Assess the morphology of the red blood cells.
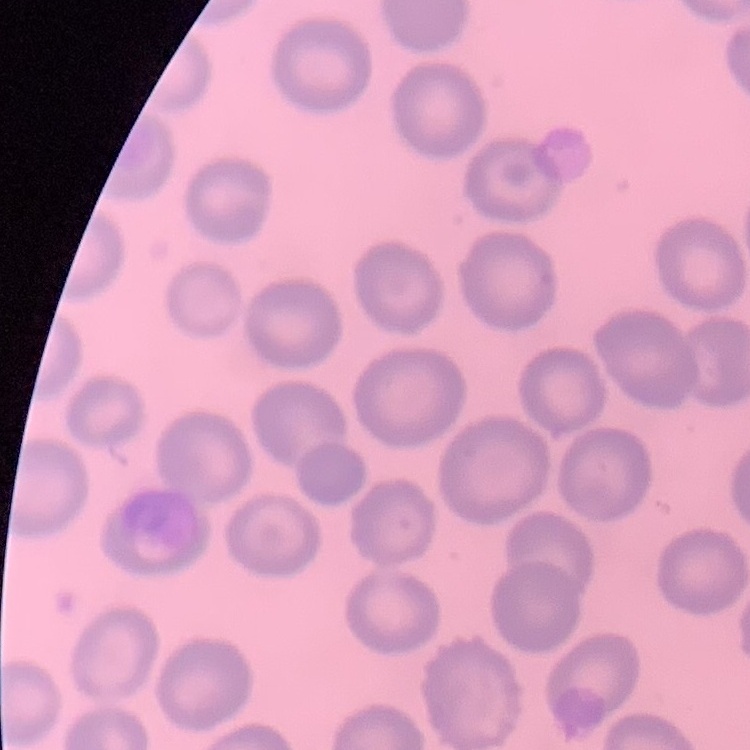
They show no rouleaux formation.

Field's or Giemsa stain. Thin peripheral smear. Square crop of a larger photomicrograph.